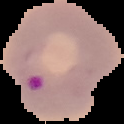

Summary:
  - Result: malaria parasites identified
  - Preparation: thin blood film
  - Image type: segmented cell region with the area outside set to black
  - Image size: 124×124 pixels